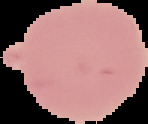
Malaria status: uninfected. Cell region segmented out of the field of view; the surrounding area is masked to black. From a thin blood film. Image is 148×124 pixels.